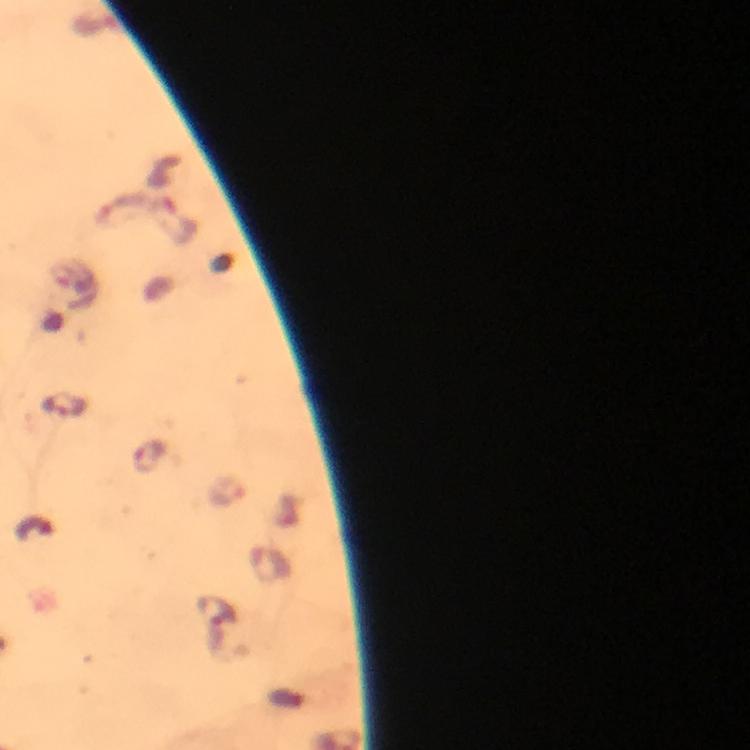
preparation = thick blood smear
immersion oil = applied
capture = smartphone mounted on the microscope
image size = 750×750 pixels
magnification = 100x
stain = Giemsa
cropped from = one field of view
context = from a diagnostic examination for malaria
Plasmodium parasite locations = approximate object centers, in pixels from the top-left corner: (x=63, y=405), (x=230, y=491)